Classify this cell by malaria status.
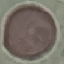
Uninfected.

preparation = thin blood film
capture = smartphone camera at the microscope eyepiece
image type = automatically extracted cell patch, resized to 64 × 64 pixels
stain = Giemsa